Identify the preparation type.
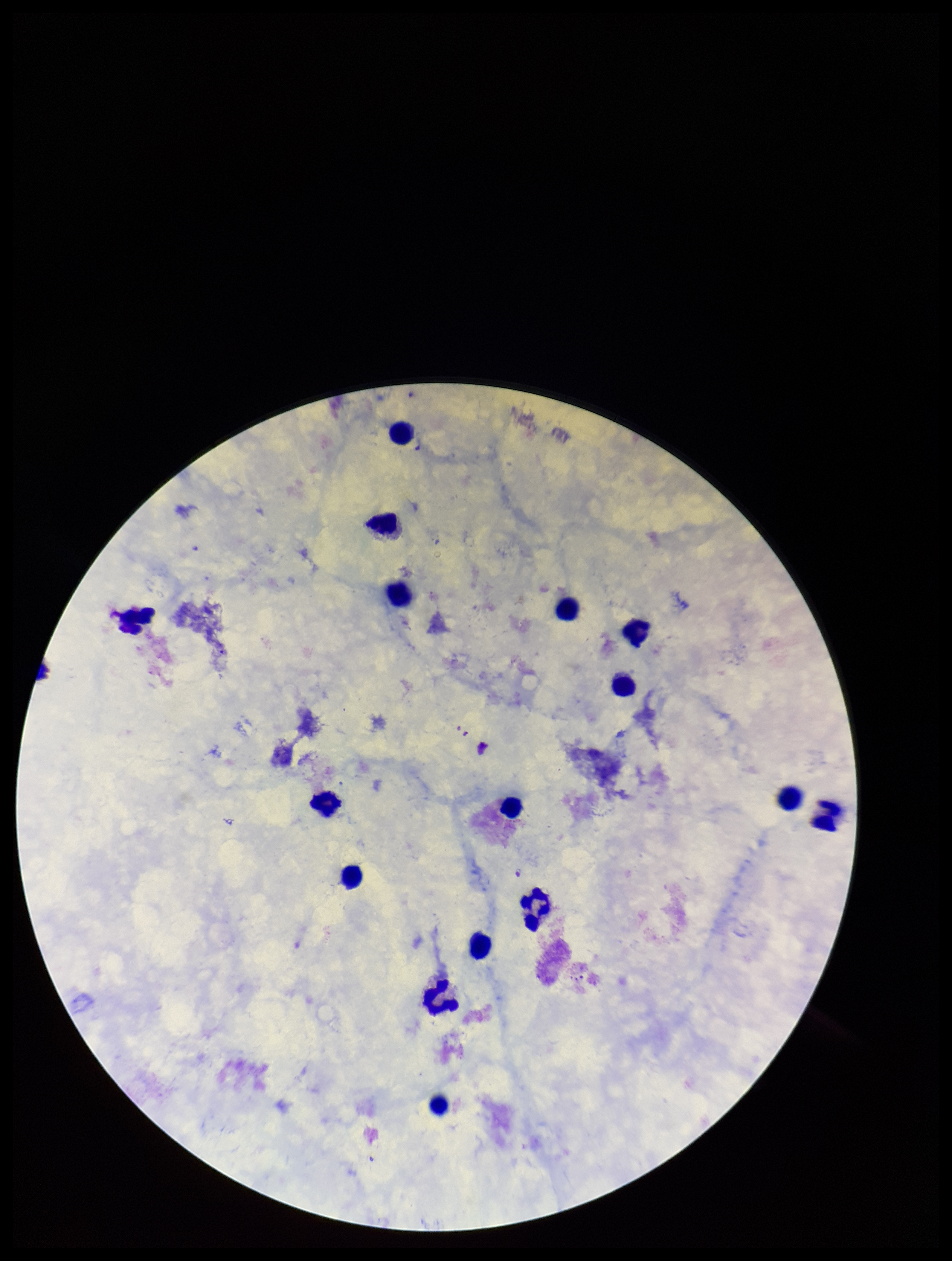
It is a thick blood smear.

{
  "patient_malaria_status": "positive",
  "stain": "Giemsa",
  "leukocyte_count": 16,
  "field_of_view": "single",
  "image_size": "952×1261 pixels",
  "plasmodium_parasites": "none detected",
  "species_reported_for_this_patient": "Plasmodium falciparum",
  "capture": "smartphone photograph through the microscope eyepiece",
  "parasite_count": 0
}